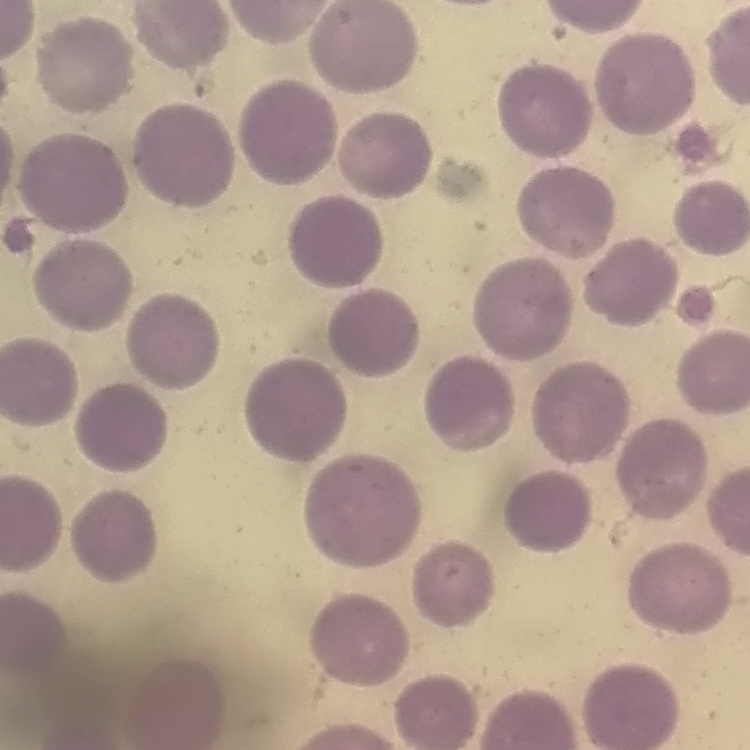

red blood cell morphology = no rouleaux formation
stain = Field's or Giemsa
image type = one tile cut from a larger photomicrograph
preparation = thin peripheral smear